Find the cells and give the type of each one.
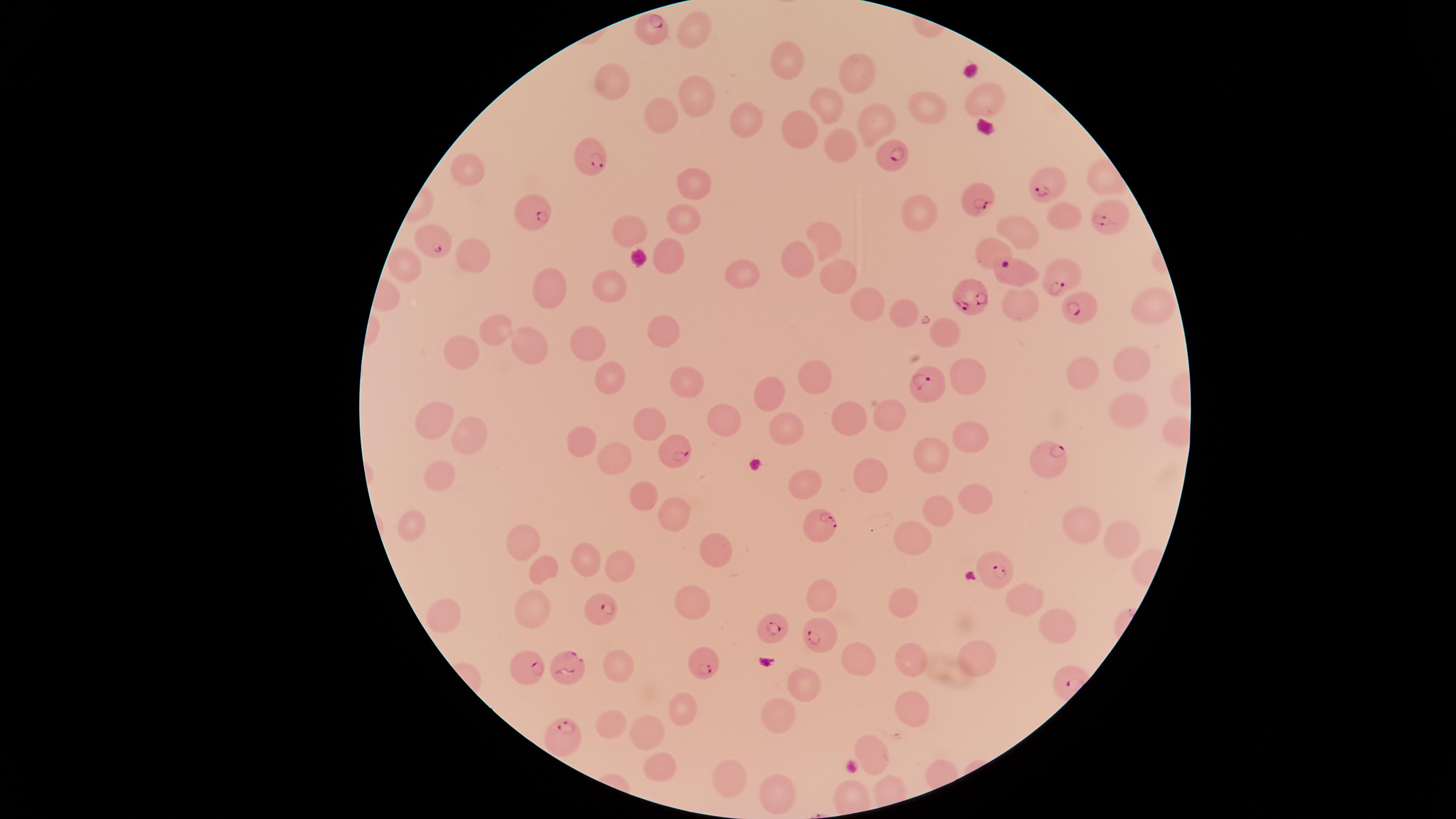
Approximate marker points as (x, y) in pixels.
Parasitized RBCs: (655, 29), (593, 157), (888, 159), (1039, 187), (975, 200), (532, 214), (1108, 216), (436, 242), (1062, 281), (972, 297), (1077, 312), (930, 385), (675, 451), (1047, 457), (820, 525), (990, 571), (599, 609), (771, 625), (819, 637), (701, 661), (570, 668), (531, 671), (559, 735).
Uninfected RBCs: (689, 27), (790, 66), (859, 69), (614, 82), (698, 96), (826, 100), (984, 101), (666, 113), (929, 113), (744, 117), (872, 122), (800, 125), (842, 143), (468, 170), (692, 180), (1059, 212), (914, 216), (685, 217), (631, 229), (1018, 231), (828, 240), (991, 248), (667, 254), (794, 259), (470, 260), (402, 265), (840, 274), (742, 276), (606, 284), (546, 286), (861, 300), (1017, 303), (1145, 304), (896, 308), (491, 330), (665, 332), (940, 333), (588, 344), (532, 346), (466, 347), (1128, 363), (966, 368), (818, 370), (1080, 372), (607, 375), (686, 379), (762, 392), (1125, 401), (724, 413), (853, 413), (892, 414), (651, 419), (432, 425), (779, 425), (966, 433), (472, 435), (586, 440), (614, 455), (927, 455), (871, 473), (803, 479), (437, 484), (645, 489), (974, 498), (936, 512), (673, 520), (1087, 521), (412, 523), (1120, 537), (525, 540), (911, 542), (719, 543), (590, 555), (620, 565), (536, 567), (1027, 594), (820, 596), (904, 601), (530, 608), (444, 609), (692, 609), (1060, 624), (975, 652), (910, 658), (861, 659), (614, 667), (804, 682), (684, 707), (920, 710), (779, 716), (609, 724), (652, 730), (871, 748), (662, 767), (728, 783), (777, 789).
No WBCs identified.

{
  "capture": "smartphone photograph through the microscope eyepiece",
  "visible_region": "circular",
  "species": "Plasmodium falciparum",
  "stain": "Giemsa",
  "field_of_view": "single",
  "preparation": "thin smear of blood",
  "image_size": "1456×819 pixels"
}